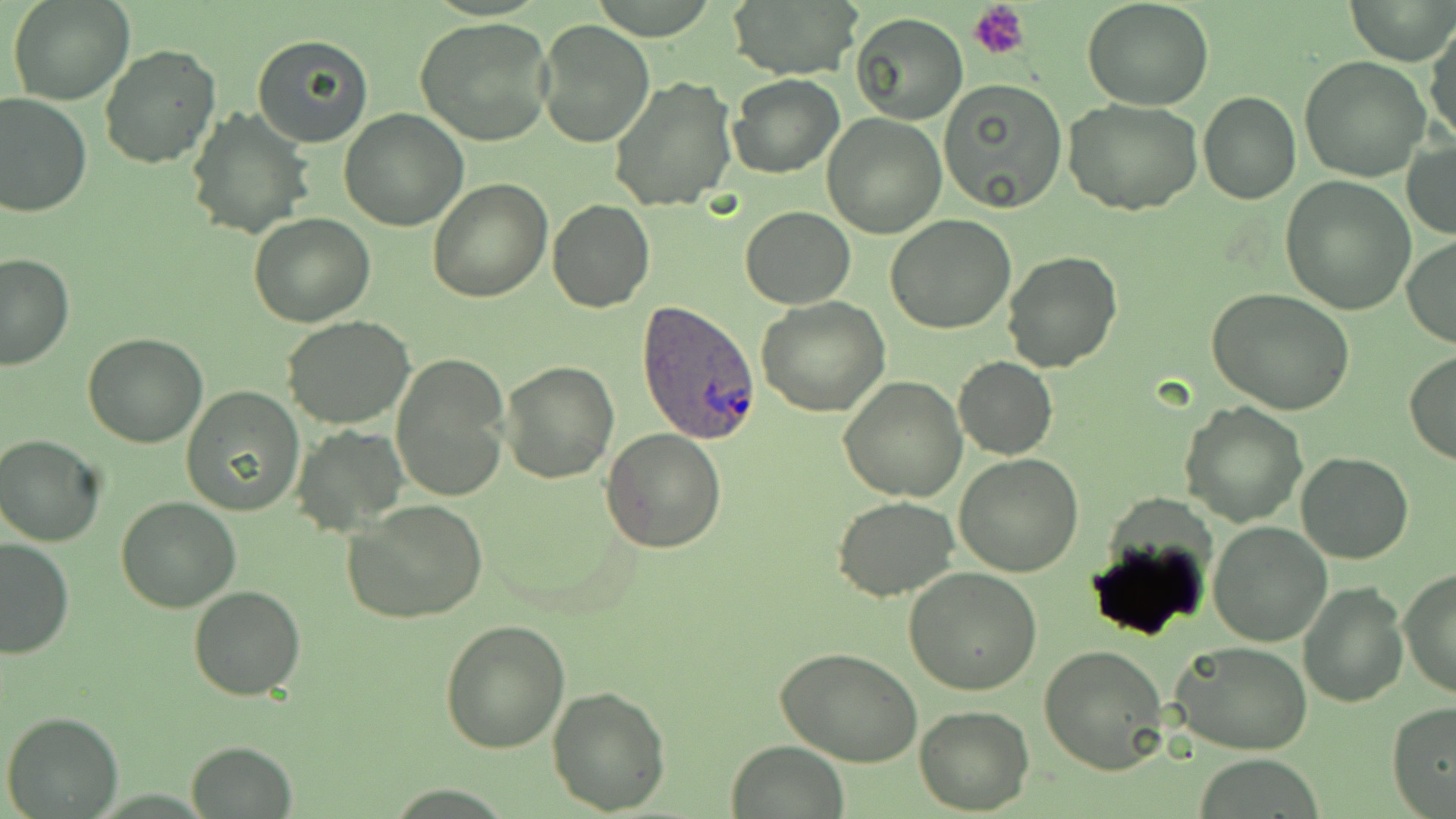
{
  "slide_level_diagnosis": "Plasmodium ovale",
  "uninfected_red_blood_cell_locations": "approximate bounding boxes as (x1, y1, x2, y2) in pixels: (8, 0, 132, 105), (723, 0, 861, 81), (1083, 0, 1214, 110), (1347, 0, 1455, 65), (849, 12, 967, 124), (415, 18, 555, 147), (534, 19, 655, 149), (1426, 21, 1456, 147), (252, 33, 376, 149), (99, 43, 220, 170), (1300, 56, 1431, 181), (728, 73, 845, 179), (609, 75, 739, 210), (940, 79, 1069, 213), (1199, 91, 1301, 203), (0, 93, 92, 217), (1064, 97, 1203, 215), (186, 107, 313, 239), (339, 109, 468, 230), (822, 114, 947, 238), (1403, 139, 1456, 239), (1280, 177, 1416, 314), (427, 178, 552, 301), (547, 200, 656, 313), (739, 206, 854, 309), (249, 213, 376, 328), (885, 216, 1017, 334), (1403, 235, 1456, 347), (1001, 250, 1124, 373), (0, 253, 74, 371), (1205, 288, 1354, 415), (755, 296, 890, 418), (280, 316, 415, 429), (82, 332, 207, 448), (1404, 352, 1456, 465), (392, 355, 509, 500), (954, 356, 1057, 460), (500, 359, 619, 483), (837, 376, 968, 501), (182, 386, 305, 516), (1180, 401, 1307, 526), (291, 425, 410, 536), (601, 429, 727, 554), (1, 433, 108, 546), (1297, 451, 1413, 564), (953, 454, 1084, 576), (115, 495, 241, 613), (833, 495, 960, 602), (343, 499, 490, 626), (1207, 522, 1331, 646), (0, 537, 74, 659), (1085, 537, 1212, 641), (903, 567, 1043, 696), (1399, 570, 1456, 699), (1298, 579, 1407, 706), (188, 583, 306, 700), (440, 620, 571, 754), (1172, 640, 1315, 754), (1039, 644, 1170, 774), (777, 646, 922, 768), (546, 685, 672, 814), (1386, 702, 1456, 818), (914, 707, 1035, 814), (2, 710, 124, 819), (187, 739, 297, 817), (727, 739, 851, 819)",
  "plasmodium_ovale_infected_red_blood_cell_locations": "approximate bounding boxes as (x1, y1, x2, y2) in pixels: (637, 299, 764, 444)",
  "stain": "May-Grünwald-Giemsa",
  "image_size": "1456×819 pixels",
  "magnification": "1000x",
  "field_of_view": "one of a larger specimen",
  "modality": "light microscopy",
  "preparation": "thin blood film",
  "platelet_locations": "approximate bounding boxes as (x1, y1, x2, y2) in pixels: (970, 1, 1030, 60)"
}